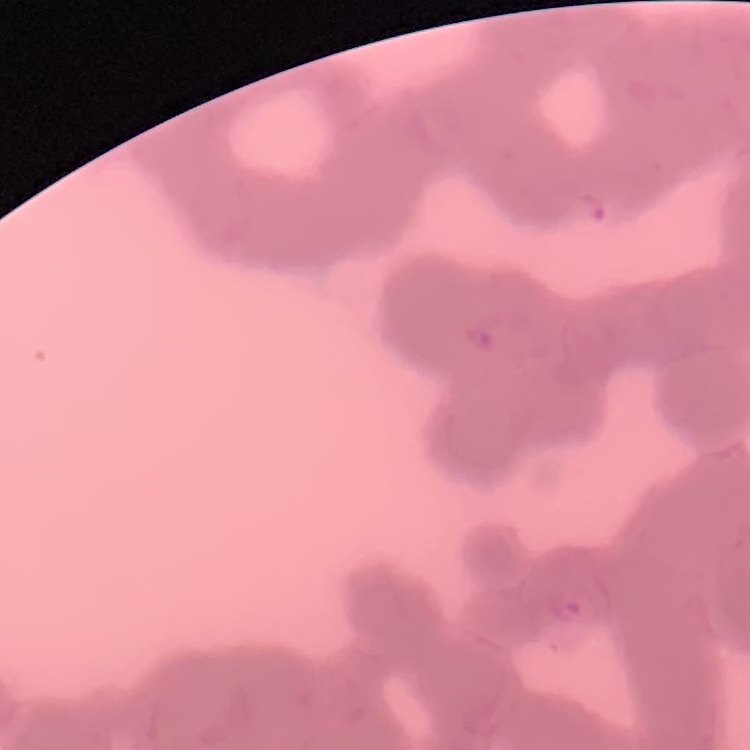
Summary:
  - Erythrocyte morphology: rouleaux formation
  - Preparation: thin peripheral smear
  - Image type: square crop of a larger photomicrograph
  - Stain: Field's or Giemsa